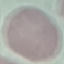
Malaria status: uninfected. Acquired by smartphone through the microscope eyepiece. Giemsa-stained preparation. Automatically extracted cell patch, resized to 64 × 64 pixels. Thin blood smear.